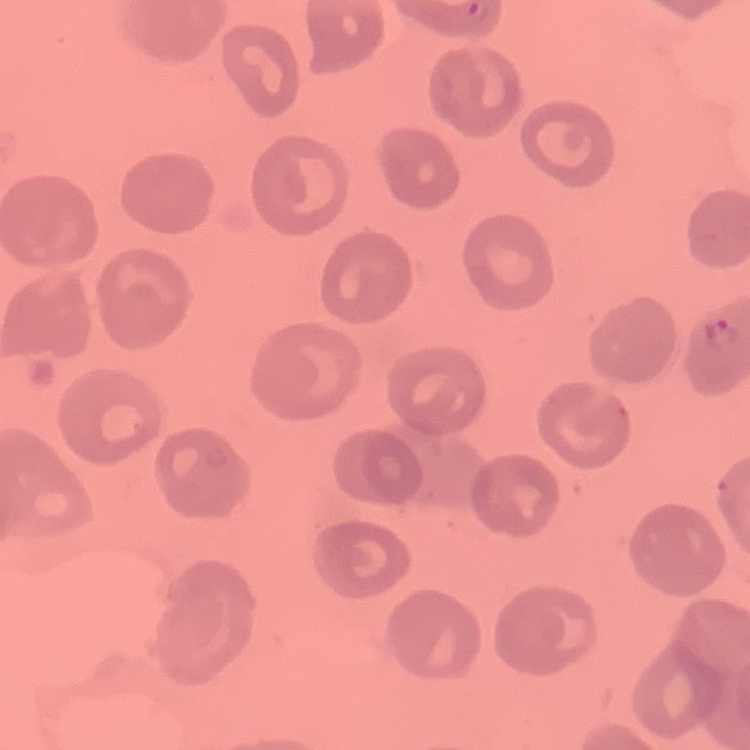
red blood cell morphology = no rouleaux formation
preparation = thin peripheral smear
image type = square crop of a larger photomicrograph
stain = Field's or Giemsa